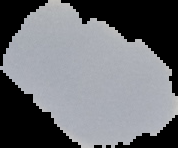 Result: negative for malaria parasites. From a thin blood smear. Image is 178×148 pixels. Segmented cell region on a black background.